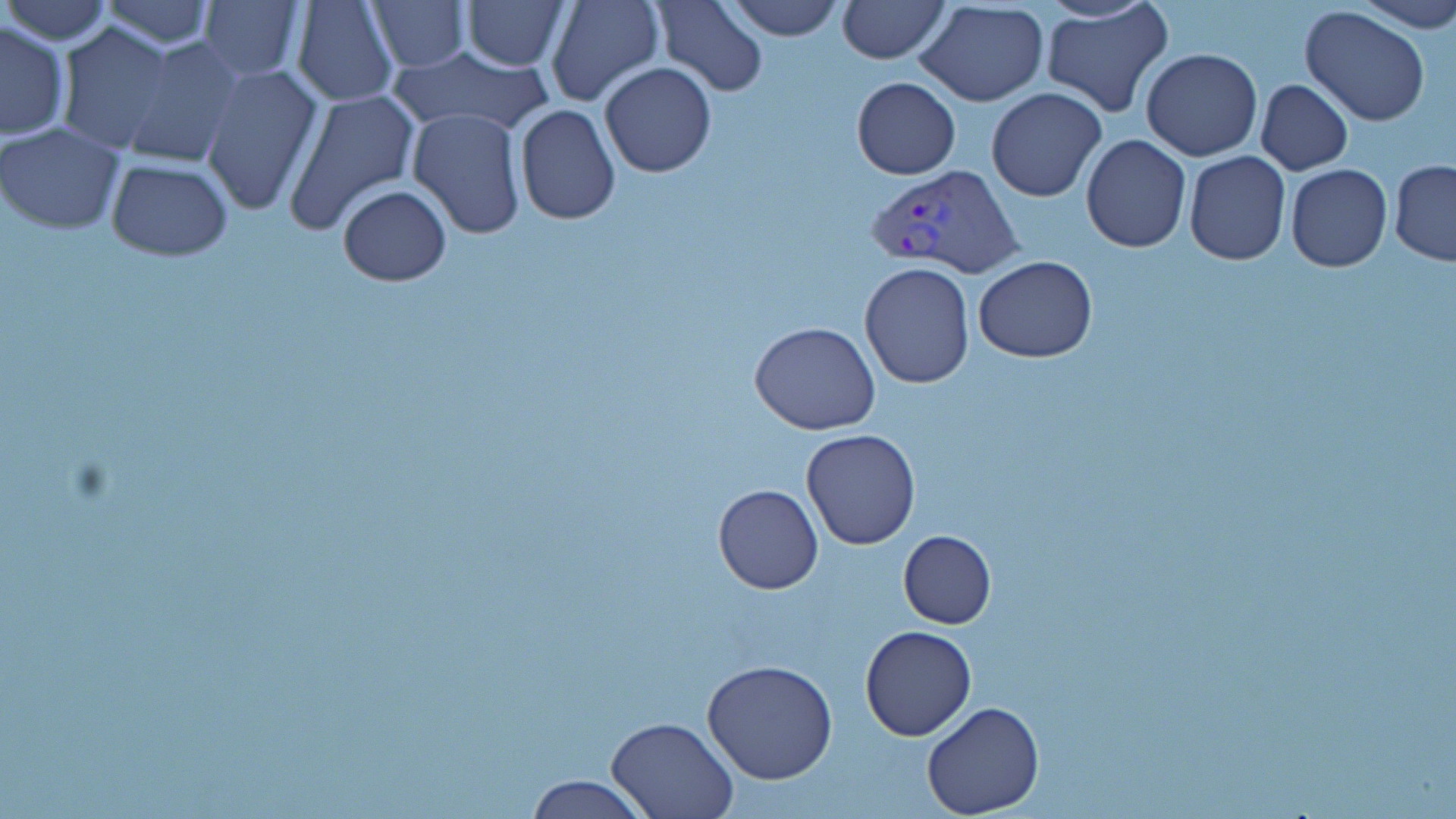
Approximate bounding boxes as (x1,y1)-(x2,y2) corner pairs in pixels. Plasmodium vivax-infected red blood cell locations: (864,161)-(1023,276). Uninfected red blood cell locations: (4,0)-(114,45), (311,0)-(498,98), (367,0)-(470,70), (728,0)-(842,40), (838,0)-(949,63), (1351,0)-(1456,34), (97,1)-(218,49), (291,1)-(398,107), (462,1)-(566,70), (544,1)-(665,107), (651,1)-(768,95), (198,2)-(305,82), (915,3)-(1050,107), (1041,3)-(1174,118), (1300,5)-(1431,128), (1,20)-(70,139), (55,23)-(179,154), (119,37)-(243,169), (386,43)-(555,141), (1141,48)-(1263,161), (599,61)-(716,177), (200,64)-(323,217), (851,76)-(960,179), (1255,79)-(1353,175), (986,86)-(1106,202), (287,88)-(421,231), (513,103)-(621,224), (406,106)-(527,238), (0,121)-(126,235), (1080,136)-(1191,254), (1183,151)-(1291,266), (105,160)-(233,261), (1389,160)-(1456,267), (1284,163)-(1392,272), (337,185)-(451,286), (973,255)-(1097,363), (859,262)-(976,389), (750,320)-(880,435), (800,429)-(922,549), (713,483)-(822,594), (897,530)-(995,629), (859,625)-(976,741), (702,659)-(838,785), (920,701)-(1046,819), (608,717)-(736,819), (524,775)-(652,818). Slide-level diagnosis: Plasmodium vivax. Single field of view. Image is 1456×819 pixels. 1000x magnification. Optical microscopy. Thin blood film. May-Grünwald-Giemsa stain.